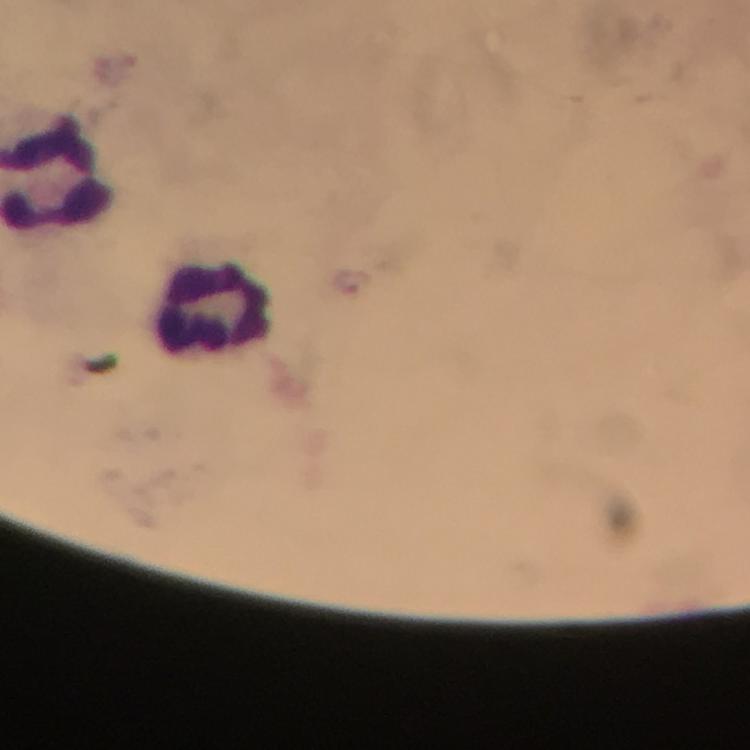

stain: Giemsa
preparation: thick smear
cropped_from: one field of view
plasmodium_parasites: none detected
capture: smartphone camera through the microscope
context: from a malaria diagnostic workup
leukocyte_locations: 'approximate centers as {x, y} in pixels: {215, 309}'
magnification: 100x
image_size: 750×750 pixels
immersion_oil: applied